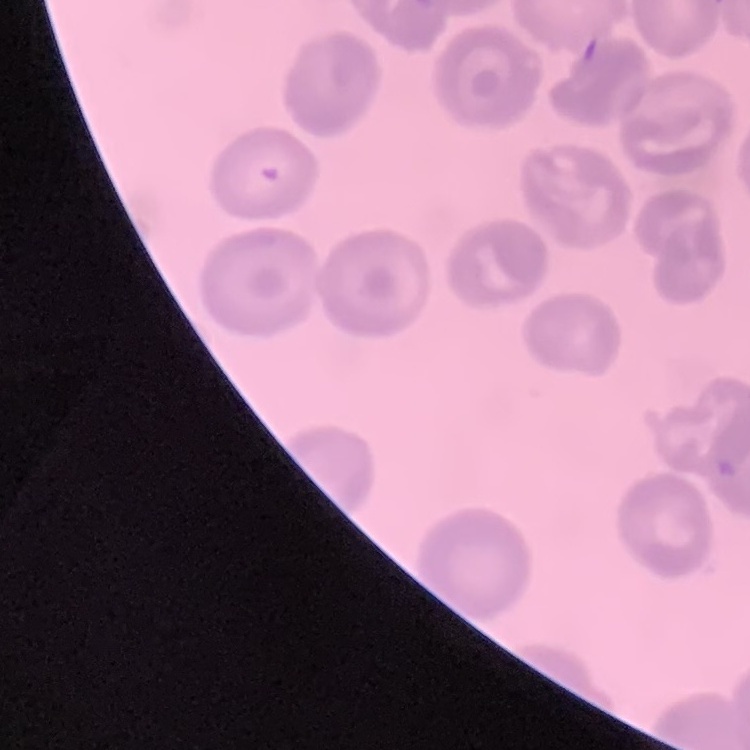
Summary:
  - Red blood cell morphology: no rouleaux formation
  - Image type: one tile cut from a larger photomicrograph
  - Stain: Field's or Giemsa
  - Preparation: thin blood smear